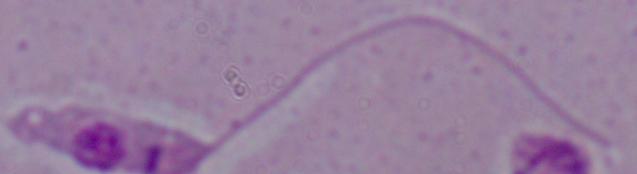

modality = photomicrograph
identification = Leishmania
magnification = 1000x